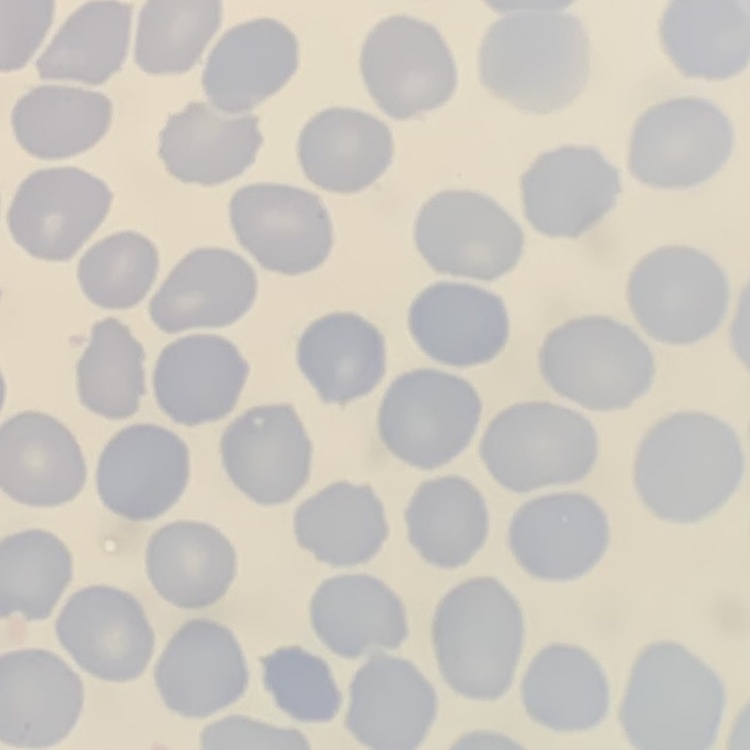

red_blood_cell_morphology: no rouleaux formation
stain: Field's or Giemsa
preparation: thin blood smear
image_type: one tile cut from a larger photomicrograph